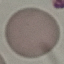

malaria status = uninfected
image type = cell patch, automatically extracted from a larger field of view and resized to 64 × 64 pixels
capture = smartphone camera at the microscope eyepiece
preparation = thin smear
stain = Giemsa